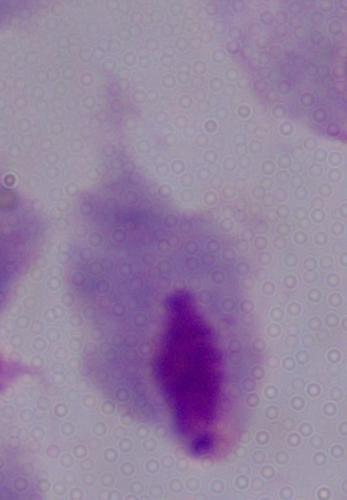
Summary:
  - Modality: photomicrograph
  - Magnification: 1000x
  - Identification: trichomonad